Point out malaria parasites and leukocytes.
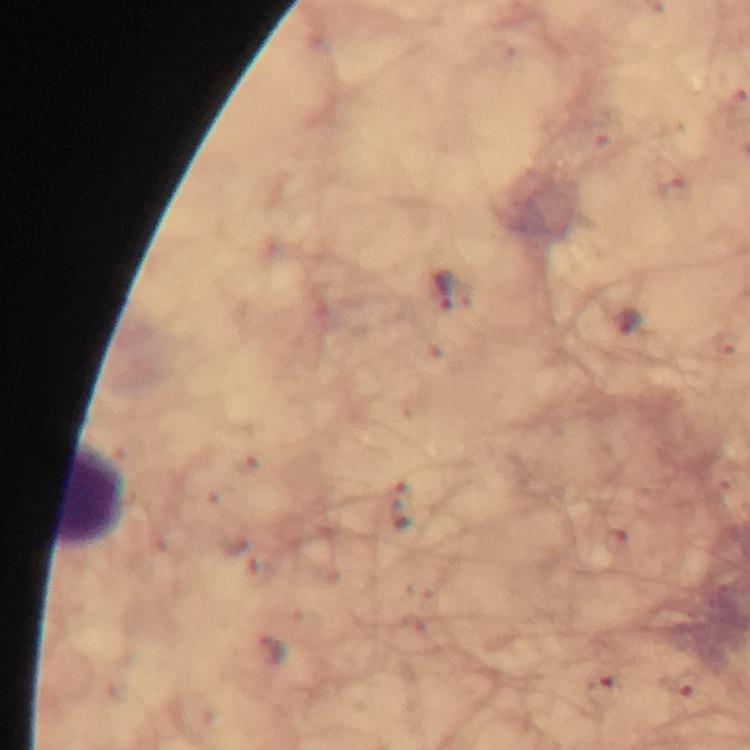
Approximate object centers, in pixels from the top-left corner.
Malaria parasites: (x=444, y=290), (x=404, y=506), (x=684, y=683), (x=606, y=690).
Leukocytes: (x=91, y=498).

preparation = thick blood film
cropped from = one field of view
image size = 750×750 pixels
stain = Giemsa
magnification = 100x
capture = smartphone photograph through a microscope
context = from a diagnostic examination for malaria
immersion oil = applied